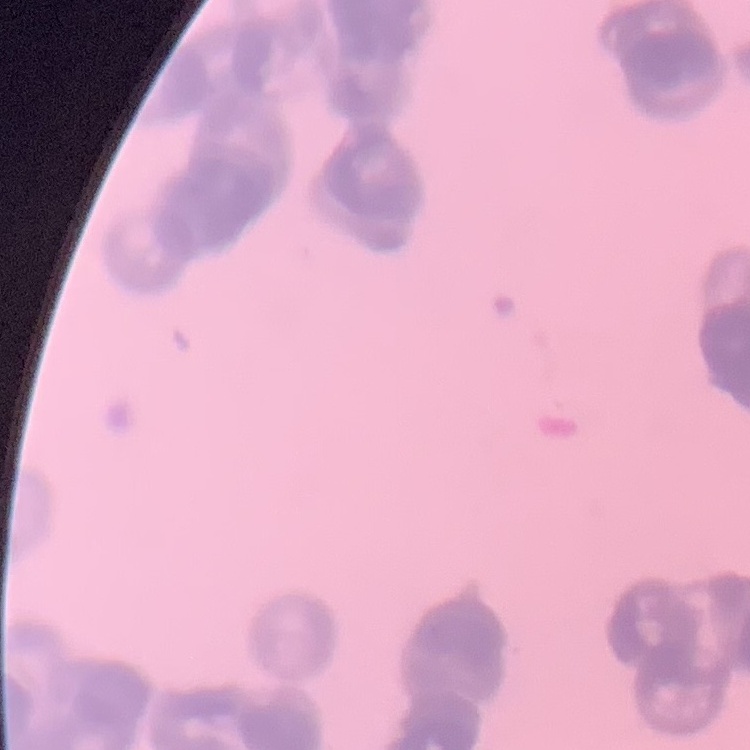
The red blood cells show rouleaux formation. One tile cut from a larger photomicrograph. Thin blood film. Field's or Giemsa stain.